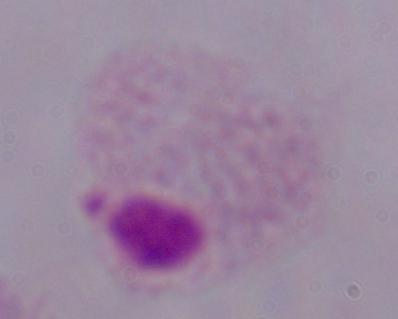

1000x magnification. A trichomonad is shown. Micrograph.